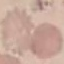
Result: negative for malaria parasites. Photographed with a smartphone camera at the microscope eyepiece. Thin blood smear. Automatically extracted cell patch, resized to 64 × 64 pixels. Giemsa-stained preparation.